Locate platelets.
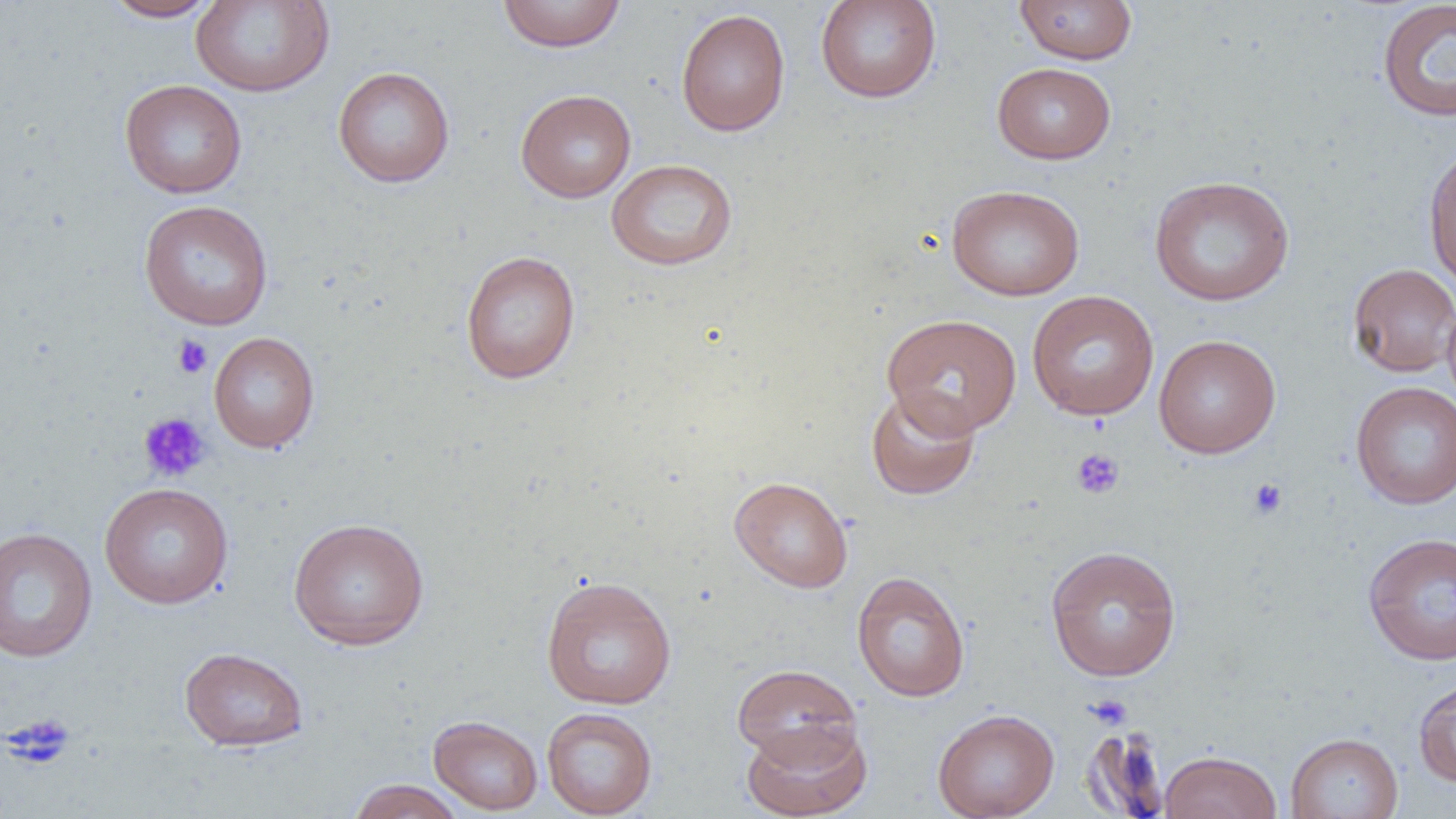
Approximate bounding boxes as (x1, y1, x2, y2) in pixels.
Platelets: (172, 335, 213, 378), (138, 412, 211, 483), (1071, 448, 1125, 500), (1247, 477, 1288, 520), (1085, 694, 1133, 729), (4, 712, 76, 769).

Uninfected red blood cell locations: (102, 0, 223, 22), (190, 0, 335, 97), (497, 0, 626, 52), (814, 0, 943, 103), (1014, 1, 1138, 65), (1377, 1, 1456, 122), (676, 8, 791, 137), (991, 62, 1116, 165), (333, 66, 455, 188), (119, 79, 248, 199), (515, 88, 636, 203), (1422, 144, 1456, 292), (606, 158, 738, 270), (1148, 175, 1295, 306), (946, 185, 1085, 301), (138, 199, 274, 330), (460, 250, 581, 384), (1347, 262, 1456, 377), (1026, 290, 1159, 421), (1442, 294, 1456, 414), (882, 313, 1022, 437), (208, 331, 320, 453), (1153, 333, 1281, 459), (1350, 381, 1456, 509), (865, 386, 982, 500), (729, 475, 853, 593), (99, 482, 234, 609), (287, 517, 430, 651), (0, 527, 98, 662), (1363, 532, 1456, 665), (1045, 544, 1182, 682), (851, 571, 970, 702), (540, 576, 677, 710), (179, 646, 309, 752), (732, 663, 861, 766), (1413, 678, 1456, 787), (541, 707, 658, 818), (932, 708, 1060, 819), (428, 715, 543, 815), (741, 718, 873, 819), (1078, 725, 1172, 817), (1285, 732, 1403, 819), (1159, 750, 1282, 819), (346, 779, 467, 819). Slide-level diagnosis: no evidence of blood parasites. Thin blood film. Light microscopy. Captured at 1000x magnification. One field of a larger specimen. Image is 1456×819 pixels.